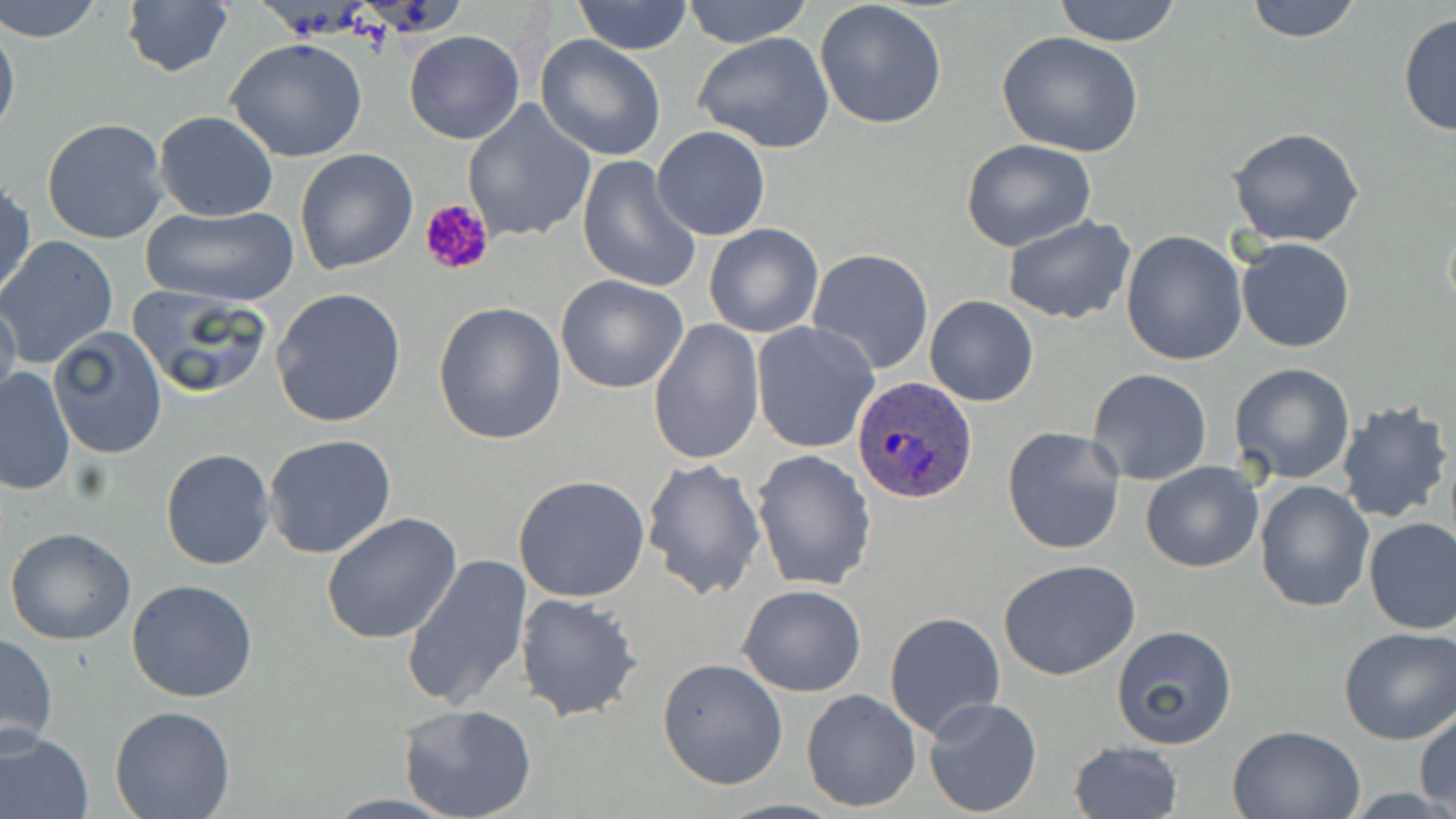

plasmodium_ovale_infected_red_blood_cell_locations: 'approximate bounding boxes as [x1, y1, x2, y2] in pixels: [852, 376, 977, 504]'
slide_level_diagnosis: Plasmodium ovale
field_of_view: one of a larger specimen
magnification: 1000x
stain: May-Grünwald-Giemsa
platelet_locations: 'approximate bounding boxes as [x1, y1, x2, y2] in pixels: [418, 197, 496, 278]'
preparation: thin blood film
image_size: 1456×819 pixels
uninfected_red_blood_cell_locations: 'approximate bounding boxes as [x1, y1, x2, y2] in pixels: [1, 0, 105, 43], [571, 0, 695, 54], [680, 0, 816, 49], [1052, 0, 1183, 46], [1242, 0, 1366, 42], [121, 1, 233, 78], [813, 2, 948, 132], [1398, 11, 1455, 137], [0, 13, 20, 146], [404, 30, 524, 145], [996, 30, 1144, 157], [693, 32, 837, 155], [537, 35, 667, 162], [226, 38, 369, 162], [462, 99, 596, 245], [153, 112, 279, 222], [41, 118, 170, 246], [651, 126, 772, 240], [1227, 127, 1366, 247], [960, 140, 1097, 252], [295, 149, 418, 275], [576, 156, 701, 294], [1, 181, 36, 304], [140, 204, 300, 308], [1003, 216, 1136, 325], [704, 223, 823, 338], [1120, 231, 1247, 367], [2, 235, 119, 367], [1236, 238, 1355, 353], [807, 248, 934, 376], [555, 274, 689, 394], [128, 285, 273, 398], [272, 289, 406, 430], [0, 295, 21, 414], [924, 295, 1038, 406], [432, 299, 567, 445], [646, 319, 762, 465], [751, 322, 879, 453], [47, 328, 168, 460], [1229, 362, 1357, 485], [1, 367, 75, 495], [1087, 368, 1212, 486], [1335, 398, 1453, 523], [1001, 426, 1127, 555], [263, 434, 397, 561], [160, 448, 275, 572], [750, 450, 876, 593], [641, 458, 765, 597], [1141, 460, 1263, 573], [512, 475, 650, 602], [1255, 480, 1375, 613], [322, 514, 464, 645], [1363, 519, 1456, 635], [4, 528, 136, 645], [400, 556, 532, 712], [999, 561, 1140, 681], [127, 580, 258, 702], [737, 584, 866, 697], [514, 592, 642, 722], [883, 610, 1006, 740], [1111, 627, 1237, 748], [1338, 627, 1456, 745], [1, 631, 58, 752], [656, 656, 787, 790], [802, 689, 921, 811], [922, 697, 1044, 819], [398, 703, 538, 819], [109, 704, 237, 819], [1414, 707, 1455, 812], [1226, 725, 1364, 818], [0, 727, 94, 819], [1068, 741, 1183, 819]'
modality: optical microscopy